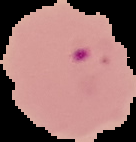
Result: malaria parasites identified. Cell region segmented out of the field of view; the surrounding area is masked to black. From a thin blood film. Image is 136×142 pixels.